Give the position of every leukocyte visible.
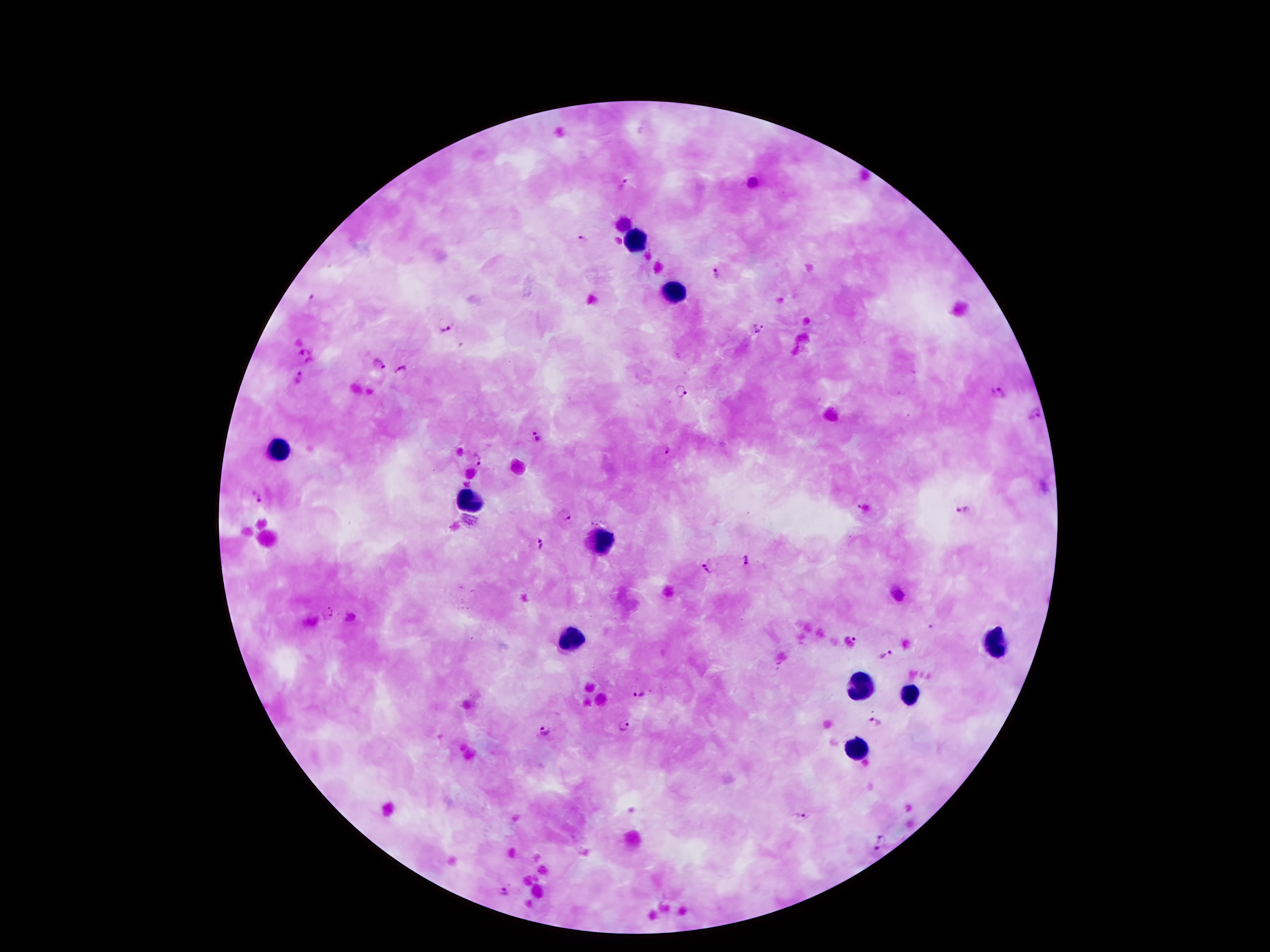
Approximate centers as {x, y} in pixels.
Leukocytes: {637, 238}, {672, 292}, {279, 450}, {465, 503}, {604, 545}, {575, 640}, {993, 644}, {863, 686}, {909, 697}, {856, 750}.

Plasmodium parasite locations = {625, 185}, {584, 239}, {717, 275}, {311, 299}, {759, 329}, {445, 331}, {307, 356}, {379, 364}, {400, 372}, {301, 377}, {682, 391}, {999, 392}, {1036, 415}, {537, 436}, {665, 451}, {481, 458}, {257, 498}, {864, 509}, {965, 510}, {566, 516}, {541, 544}, {745, 560}, {710, 567}, {855, 639}, {884, 656}, {639, 693}, {875, 723}, {624, 728}, {542, 729}, {802, 817}, {877, 841}, {504, 891}
patient malaria status = infected with Plasmodium falciparum
field of view = single
magnification = 100x
capture = smartphone through the microscope eyepiece
image size = 1270×952 pixels
stain = Giemsa
preparation = thick peripheral-blood smear